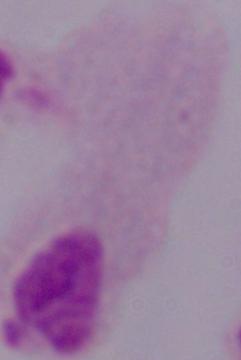
Summary:
  - Modality: photomicrograph
  - Magnification: 1000x
  - Identification: trichomonad